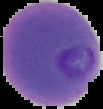

{
  "preparation": "thin blood film",
  "image_type": "cell region segmented out of the field of view; surrounding area masked to black",
  "image_size": "103×109 pixels",
  "malaria_status": "parasitized"
}